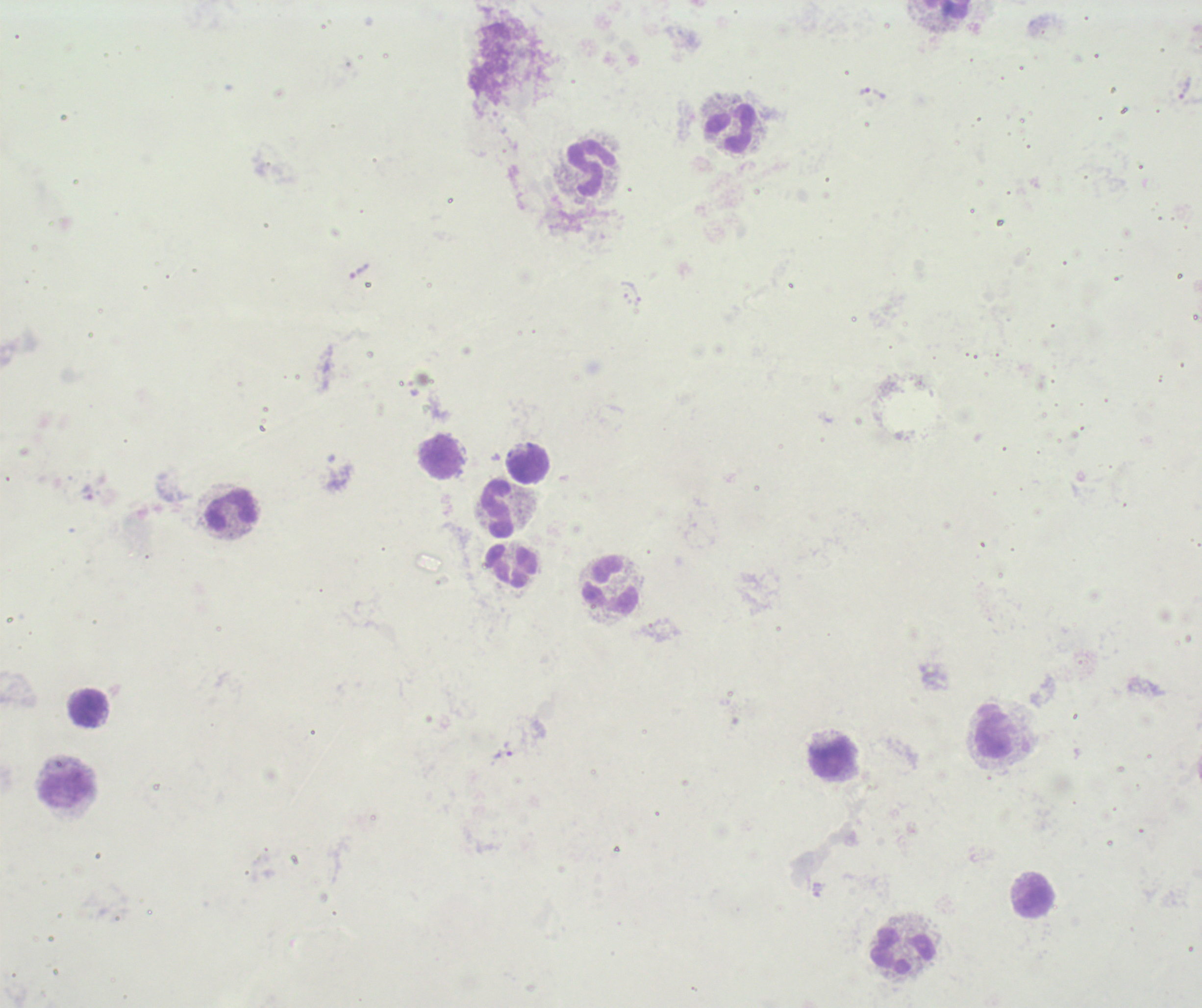
Approximate centers as {x, y} in pixels.
Summary:
  - Trophozoite locations: {864, 91}, {503, 750}
  - Leukocyte locations: {948, 10}, {731, 129}, {591, 166}, {441, 457}, {527, 463}, {498, 509}, {231, 510}, {511, 566}, {612, 585}, {89, 708}, {994, 730}, {829, 759}, {66, 789}, {1034, 896}, {904, 951}
  - Preparation: thick blood film
  - Context: previously used in an actual diagnosis
  - Stain: Romanowsky
  - Magnification: 100x
  - Result: Plasmodium parasites detected
  - Background quality: unsatisfactory
  - Field of view: single
  - Image size: 1202×1008 pixels